Assess the morphology of the red blood cells.
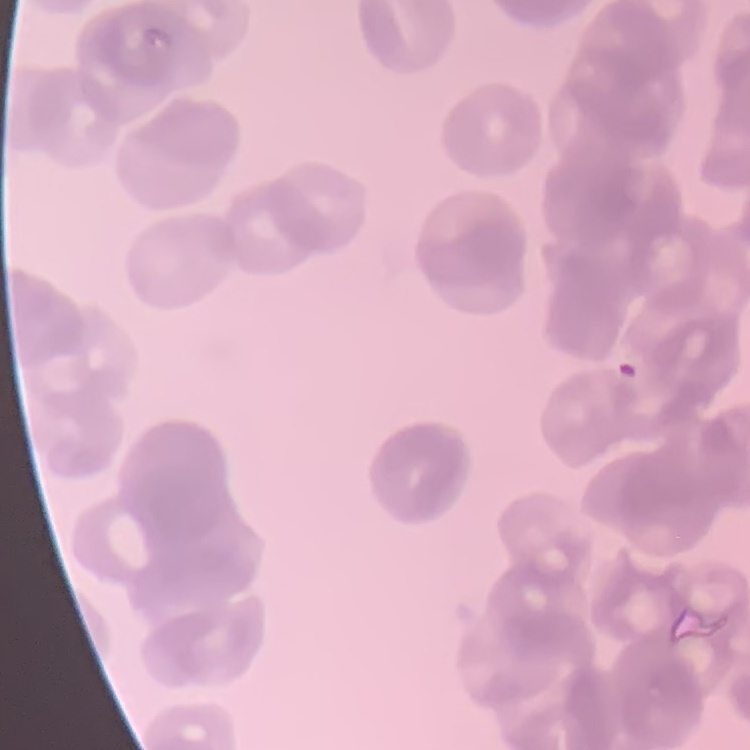

Rouleaux formation.

stain = Field's or Giemsa
image type = one tile cut from a larger photomicrograph
preparation = thin blood smear